Assess this cell for malaria.
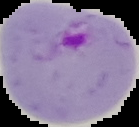
Parasitized.

From a thin blood smear. Cell region segmented out of the field of view; the surrounding area is masked to black. Image is 139×127 pixels.